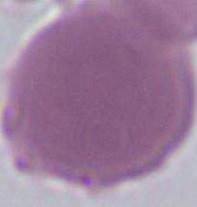 1000x magnification. An erythrocyte is seen. Micrograph.